Name the cell type shown.
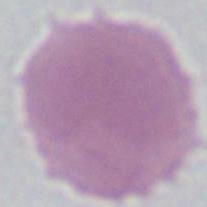
This is an erythrocyte.

Photomicrograph. Captured at 1000x magnification.